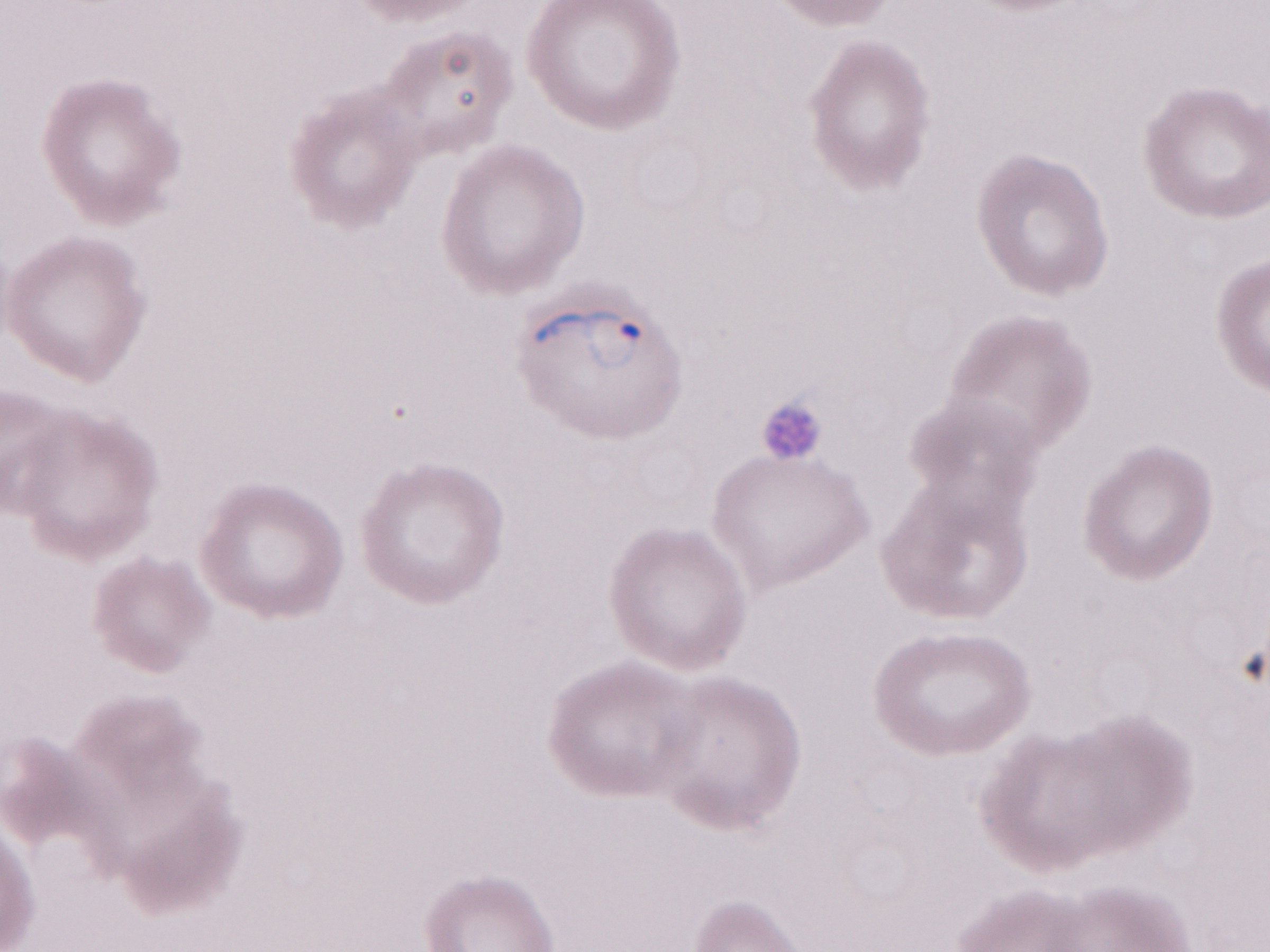 Malaria diagnosis (patient-level): positive. Olympus BX43 microscope and DP73 digital camera. Single field of view. Thin blood film. Image is 1270×952 pixels. May-Grünwald-Giemsa (MGG) stain. 1,000x magnification.